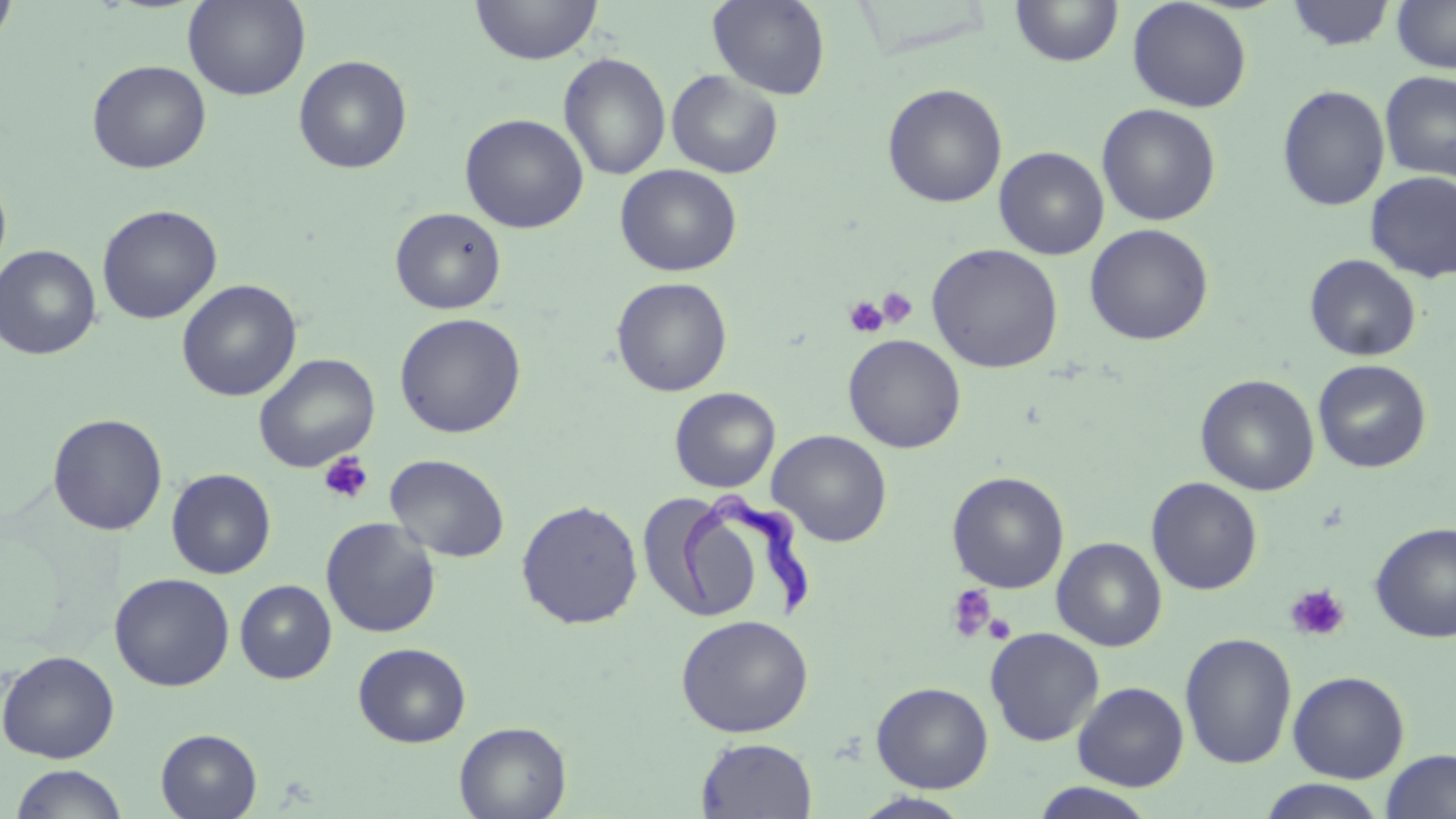

{
  "slide_level_diagnosis": "Trypanosoma brucei",
  "image_size": "1456×819 pixels",
  "trypanosoma_brucei_locations": "approximate bounding boxes as (x1, y1, x2, y2) in pixels: (678, 490, 814, 618)",
  "platelet_locations": "approximate bounding boxes as (x1, y1, x2, y2) in pixels: (876, 287, 918, 329), (843, 296, 888, 338), (319, 452, 374, 504), (1284, 583, 1350, 641), (946, 584, 998, 642), (983, 612, 1017, 645)",
  "magnification": "1000x",
  "modality": "optical microscopy",
  "field_of_view": "one of a larger specimen",
  "preparation": "thin blood smear",
  "stain": "May-Grünwald-Giemsa",
  "uninfected_red_blood_cell_locations": "approximate bounding boxes as (x1, y1, x2, y2) in pixels: (0, 0, 18, 53), (183, 0, 310, 101), (470, 0, 602, 65), (708, 0, 831, 100), (1127, 0, 1252, 112), (1391, 0, 1456, 73), (1011, 1, 1124, 68), (1285, 1, 1396, 51), (558, 53, 671, 180), (293, 55, 412, 174), (87, 59, 211, 174), (666, 70, 784, 179), (1379, 71, 1456, 182), (882, 83, 1007, 208), (1277, 84, 1391, 212), (1096, 103, 1221, 226), (459, 113, 589, 234), (994, 147, 1109, 260), (615, 164, 742, 277), (0, 167, 12, 284), (1365, 172, 1456, 283), (96, 204, 222, 324), (390, 207, 507, 314), (1084, 223, 1213, 346), (926, 243, 1064, 373), (0, 244, 101, 360), (1304, 254, 1421, 361), (611, 277, 733, 396), (176, 279, 302, 401), (394, 313, 527, 438), (843, 334, 966, 453), (253, 353, 380, 473), (1312, 359, 1432, 473), (1195, 374, 1320, 496), (669, 387, 780, 493), (47, 413, 168, 535), (768, 429, 893, 547), (385, 453, 510, 563), (166, 468, 277, 579), (946, 471, 1069, 593), (1146, 477, 1263, 595), (641, 493, 765, 621), (516, 499, 643, 629), (320, 517, 442, 639), (1370, 522, 1456, 644), (1052, 537, 1167, 651), (110, 573, 235, 691), (235, 580, 337, 683), (676, 614, 814, 737), (984, 627, 1105, 746), (1179, 631, 1297, 770), (353, 642, 470, 748), (0, 649, 120, 764), (1287, 670, 1410, 783), (871, 681, 993, 792), (1072, 681, 1189, 791), (454, 721, 572, 818), (156, 728, 262, 818), (696, 737, 817, 818), (1380, 749, 1456, 819), (9, 764, 129, 819), (1258, 779, 1387, 818), (1029, 782, 1159, 819), (851, 792, 975, 819)"
}